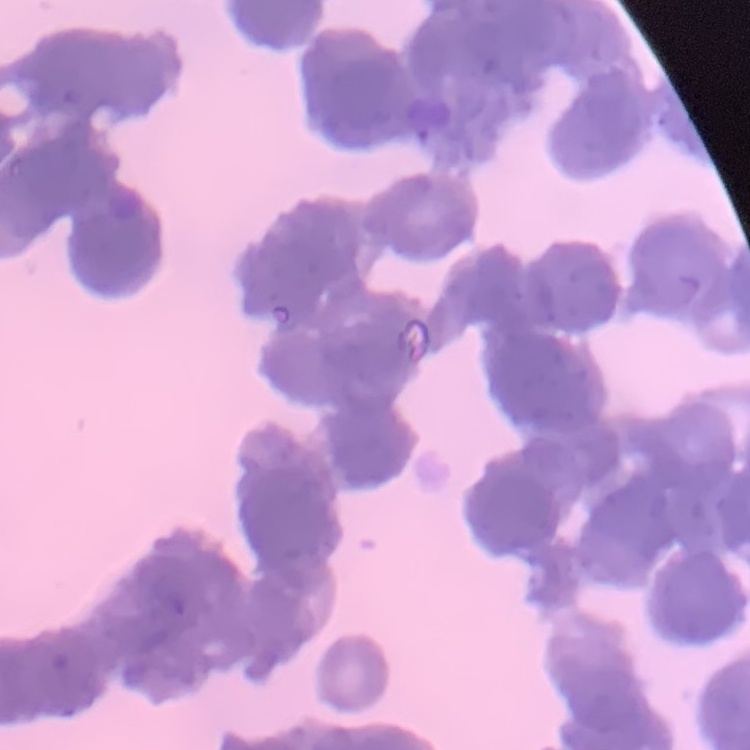
The erythrocytes show rouleaux formation. Square crop of a larger photomicrograph. Thin peripheral smear. Field's or Giemsa stain.